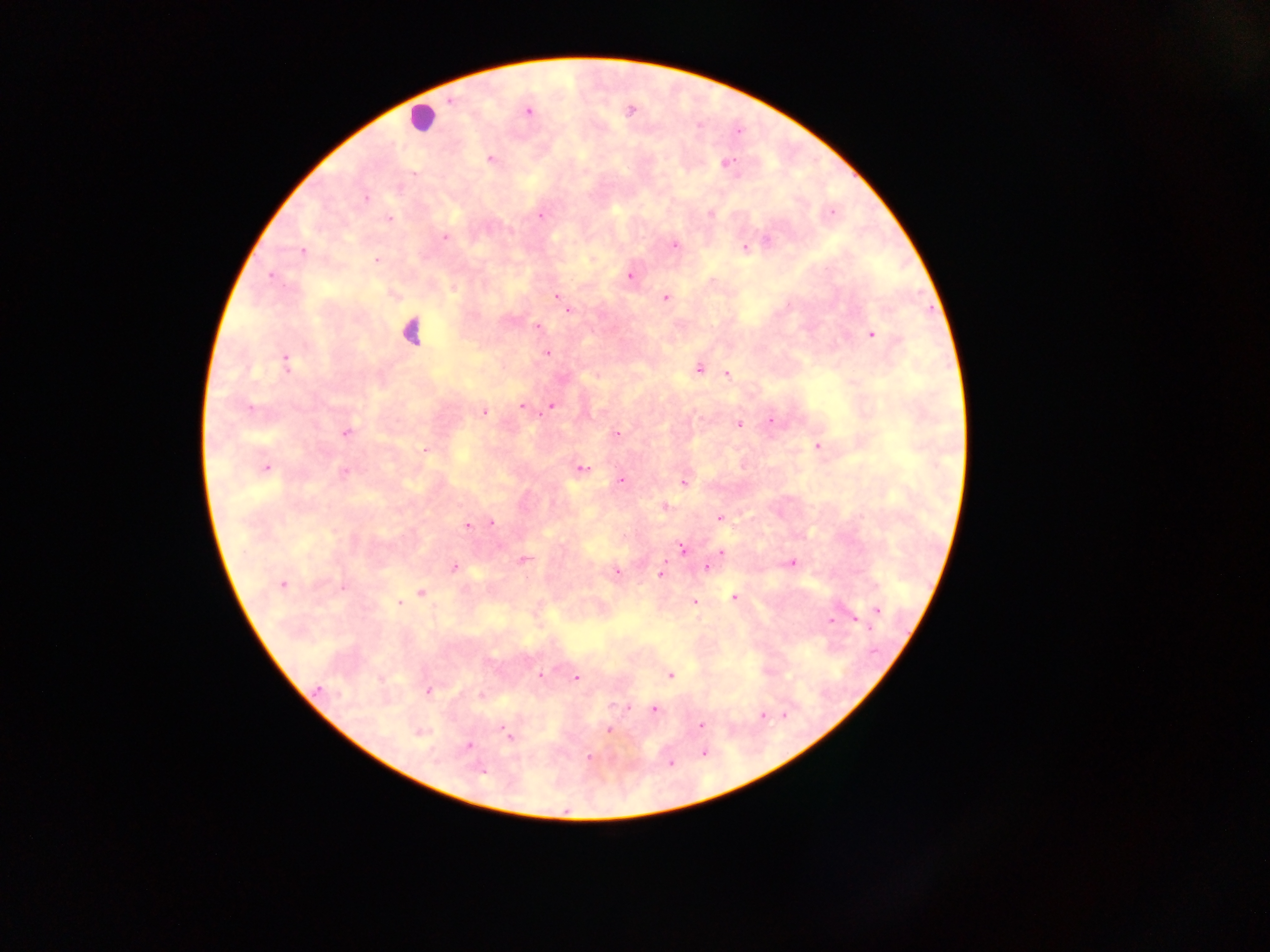 Approximate centers as x y in pixels. Plasmodium parasite locations: 630 110; 527 111; 490 159; 725 163; 365 198; 830 211; 709 212; 540 215; 388 218; 445 236; 674 244; 745 248; 302 251; 376 260; 630 274; 271 275; 454 289; 556 296; 665 297; 567 312; 536 327; 870 334; 547 352; 285 361; 698 368; 596 375; 727 375; 522 406; 550 406; 483 411; 770 421; 738 424; 345 432; 616 434; 817 446; 425 449; 264 468; 581 469; 343 471; 621 480; 683 482; 663 506; 718 518; 491 522; 467 525; 682 548; 721 553; 523 561; 791 562; 454 567; 705 567; 615 573; 661 573; 281 584; 421 592; 733 597; 693 602; 399 603; 877 610; 853 618; 830 621; 541 675; 669 675; 575 677; 428 691; 628 707; 653 709; 762 715; 701 725; 608 730; 419 732; 508 736; 468 745; 703 752; 589 757; 670 762; 481 769. Leukocyte locations: 421 117; 411 331. Thick blood film. Image is 1270×952 pixels. One field of view. Sample from Ghana. Photographed through a microscope with a mobile-phone camera.